Give the preparation type.
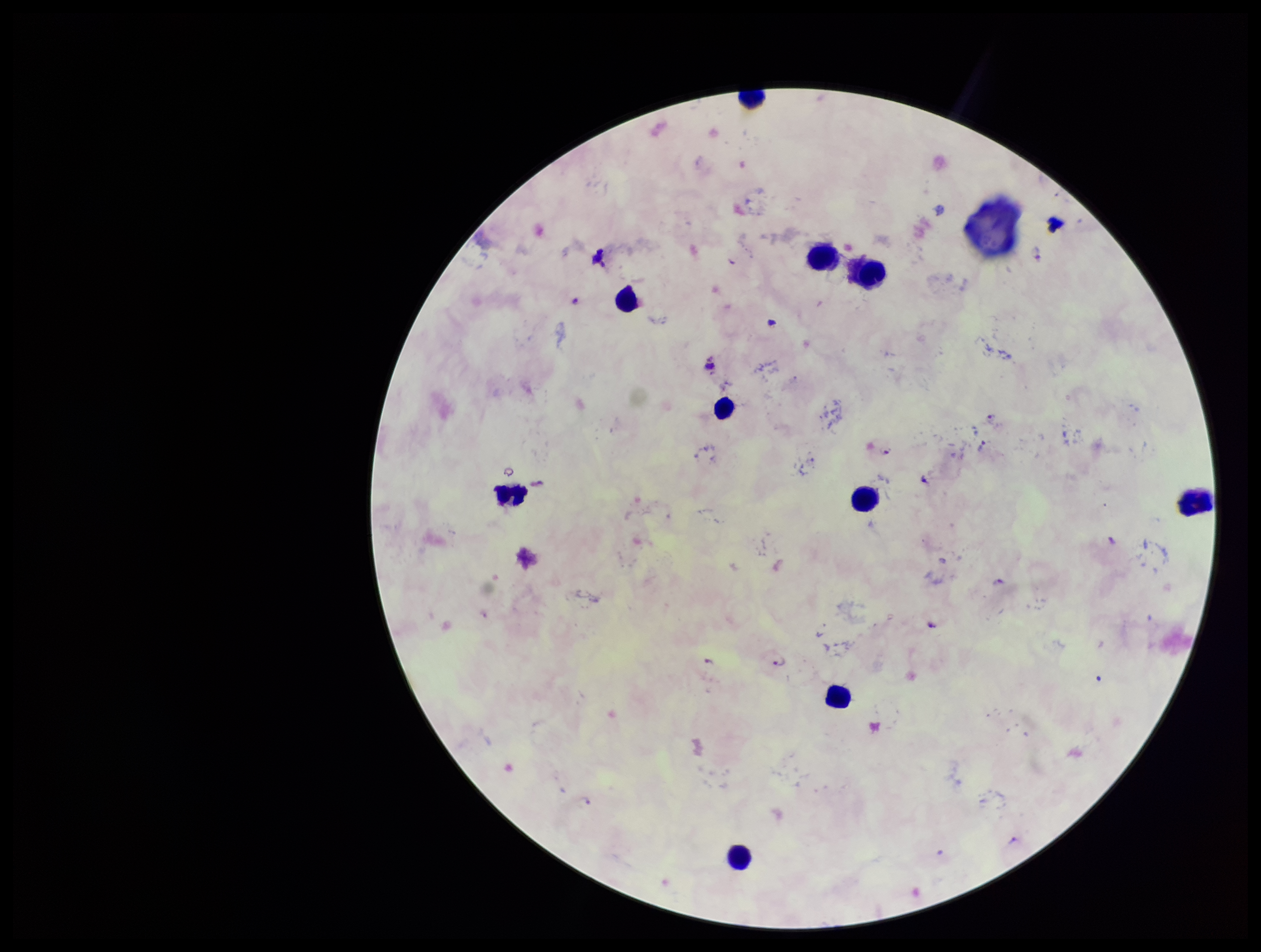
A thick smear.

plasmodium_parasites: seen
patient_malaria_status: infected
capture: smartphone photograph through the microscope eyepiece
field_of_view: single
species_reported_for_this_patient: Plasmodium falciparum
image_size: 1261×952 pixels
stain: Giemsa
parasite_count: 6
leukocyte_count: 10